State the blood parasite species.
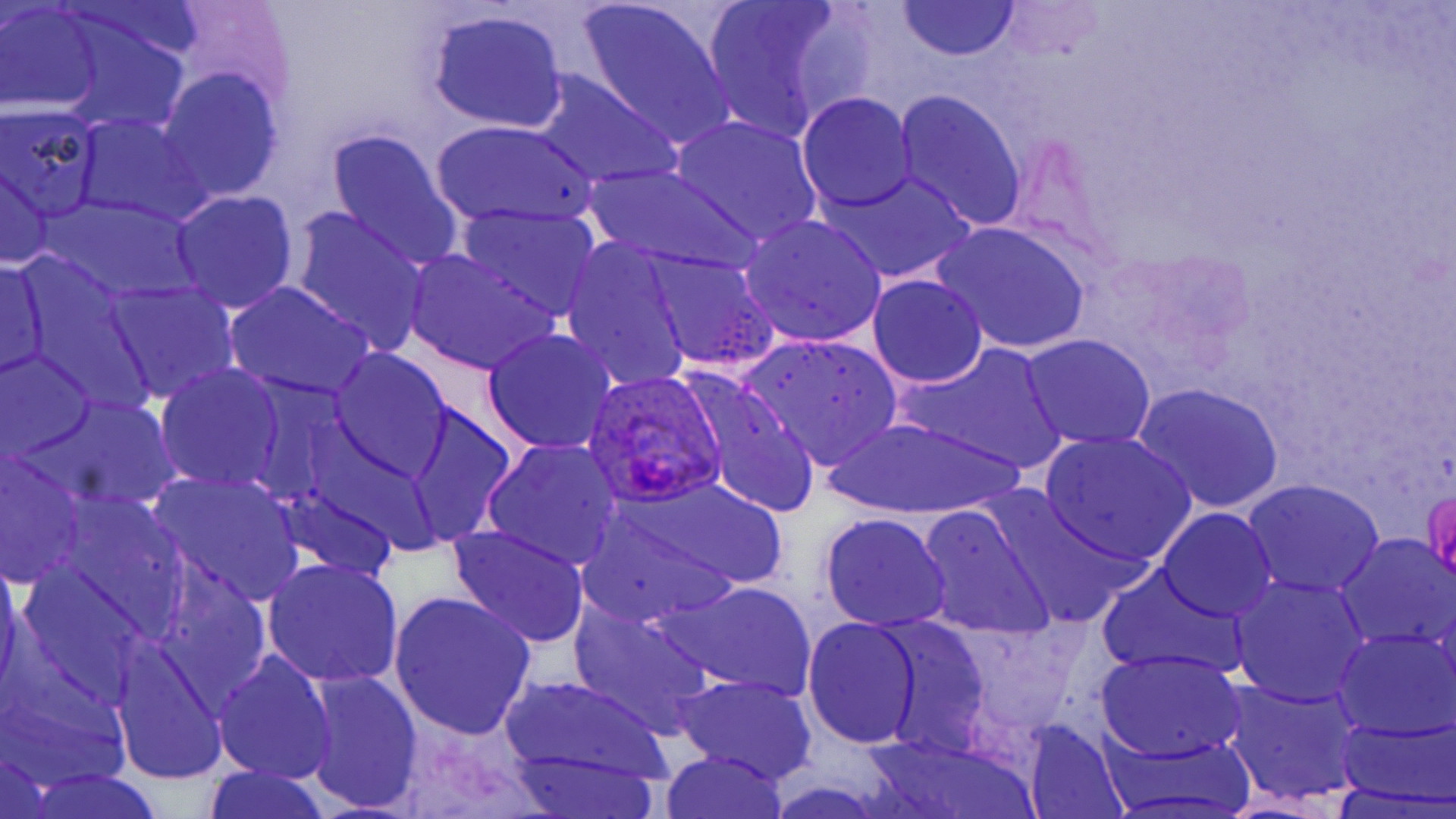

Plasmodium ovale.

Summary:
  - Coordinate format: approximate bounding boxes as (x1, y1, x2, y2) in pixels
  - Uninfected red blood cell locations: (1, 2, 106, 113), (578, 2, 738, 149), (894, 2, 1022, 61), (698, 3, 858, 140), (424, 10, 571, 133), (159, 68, 283, 200), (523, 69, 684, 190), (892, 89, 1027, 232), (798, 92, 918, 215), (1, 109, 104, 222), (75, 113, 207, 224), (668, 114, 823, 248), (432, 120, 599, 230), (327, 129, 462, 268), (586, 166, 760, 278), (822, 168, 975, 284), (0, 169, 53, 270), (170, 189, 298, 314), (288, 206, 428, 355), (455, 208, 603, 322), (738, 214, 888, 347), (930, 221, 1092, 355), (559, 238, 693, 392), (405, 249, 557, 375), (645, 249, 779, 376), (0, 256, 50, 381), (866, 273, 989, 388), (108, 281, 238, 402), (224, 281, 374, 401), (482, 328, 617, 456), (739, 334, 904, 467), (1022, 334, 1157, 452), (912, 344, 1063, 471), (329, 351, 452, 482), (0, 352, 97, 464), (155, 363, 285, 493), (687, 381, 821, 519), (1134, 382, 1285, 513), (39, 397, 180, 513), (406, 404, 517, 544), (826, 416, 1022, 521), (1039, 431, 1197, 565), (482, 439, 624, 571), (0, 453, 85, 588), (150, 472, 305, 607), (623, 475, 790, 595), (1244, 479, 1384, 597), (276, 483, 399, 584), (49, 494, 190, 633), (916, 503, 1054, 642), (1159, 508, 1277, 623), (581, 510, 745, 630), (818, 513, 953, 633), (444, 523, 591, 650), (1337, 534, 1455, 651), (260, 559, 404, 689), (14, 567, 145, 710), (1097, 567, 1245, 680), (150, 572, 272, 708), (1231, 577, 1370, 708), (665, 579, 816, 701), (391, 592, 536, 740), (570, 603, 714, 737), (803, 618, 925, 750), (879, 622, 993, 755), (1334, 628, 1455, 738), (110, 645, 228, 784), (1096, 648, 1248, 762), (213, 653, 336, 786), (305, 669, 424, 811), (501, 672, 672, 787), (671, 674, 819, 785), (1222, 680, 1363, 807), (1334, 717, 1456, 807), (1023, 723, 1125, 814), (859, 737, 1040, 819), (659, 750, 791, 818)
  - Plasmodium ovale-infected red blood cell locations: (583, 367, 727, 510)
  - Preparation: thin blood film
  - Modality: light microscopy
  - Magnification: 1000x
  - Stain: May-Grünwald-Giemsa
  - Field of view: single
  - Image size: 1456×819 pixels